Name the parasite shown.
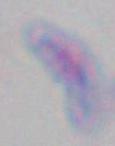

This is Toxoplasma gondii.

Summary:
  - Magnification: 1000x
  - Modality: micrograph